Find each parasitized RBC.
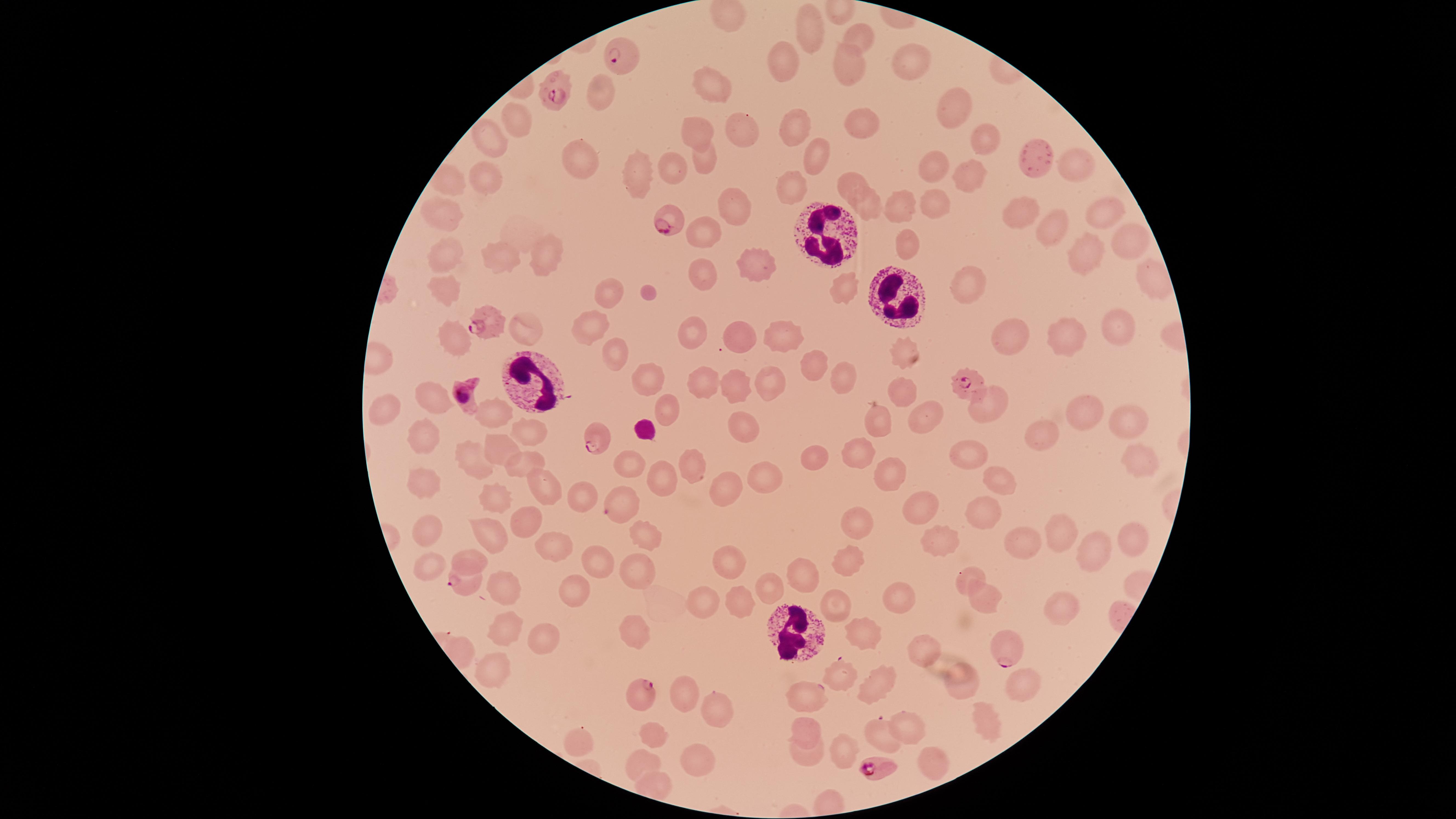

Approximate marker points as (x, y) in pixels.
Parasitized RBCs: (616, 59), (552, 95), (671, 223), (484, 322), (968, 383), (464, 398), (595, 436), (623, 501), (464, 587), (1002, 645), (839, 674), (808, 696), (644, 697), (879, 766).

image_size: 1456×819 pixels
capture: smartphone photograph through the microscope eyepiece
field_of_view: single
species: Plasmodium falciparum
preparation: thin blood smear
visible_region: circular
WBCs: 'approximate marker points as (x, y) in pixels: (830, 233), (899, 299), (525, 389), (792, 632)'
uninfected_RBCs: 'approximate marker points as (x, y) in pixels: (809, 28), (860, 38), (910, 62), (789, 66), (848, 67), (714, 84), (605, 98), (954, 104), (853, 121), (794, 126), (519, 129), (737, 132), (697, 135), (979, 138), (490, 146), (815, 157), (703, 161), (582, 164), (932, 167), (1080, 167), (672, 170), (643, 176), (966, 181), (490, 182), (848, 184), (452, 188), (793, 188), (730, 206), (902, 206), (931, 206), (868, 207), (1020, 207), (1106, 209), (446, 215), (1053, 227), (702, 235), (1126, 243), (910, 245), (1081, 247), (539, 252), (440, 256), (498, 262), (751, 262), (697, 272), (966, 283), (448, 288), (845, 289), (611, 296), (523, 326), (1117, 327), (586, 332), (785, 333), (1009, 334), (737, 336), (696, 337), (455, 338), (1063, 340), (907, 353), (617, 357), (813, 365), (653, 375), (844, 378), (703, 379), (768, 380), (730, 387), (900, 388), (431, 399), (993, 401), (385, 408), (489, 410), (1079, 412), (671, 414), (926, 417), (877, 423), (1127, 427), (746, 428), (527, 431), (1053, 435), (421, 439), (498, 448), (978, 453), (856, 460), (814, 461), (519, 462), (467, 465), (631, 465), (692, 469), (1130, 469), (999, 475), (767, 477), (890, 478), (423, 482), (659, 482), (730, 486), (544, 490), (578, 499), (497, 500), (927, 509), (983, 513), (524, 521), (859, 524), (426, 534), (643, 534), (488, 538), (1009, 538), (1063, 538), (1128, 542), (552, 543), (939, 543), (471, 557), (729, 562), (1088, 563), (848, 564), (598, 566), (430, 568), (636, 570), (966, 576), (804, 577), (504, 583), (768, 585), (573, 591), (983, 597), (894, 598), (1068, 598), (704, 600), (738, 602), (832, 604), (511, 629), (633, 631), (868, 634), (539, 640), (927, 646), (490, 667), (962, 684), (881, 688), (1012, 688), (684, 697), (711, 712), (986, 718), (907, 726), (805, 735), (881, 735), (654, 736), (577, 741), (842, 753), (806, 756), (643, 760), (696, 760), (930, 761)'
stain: Giemsa